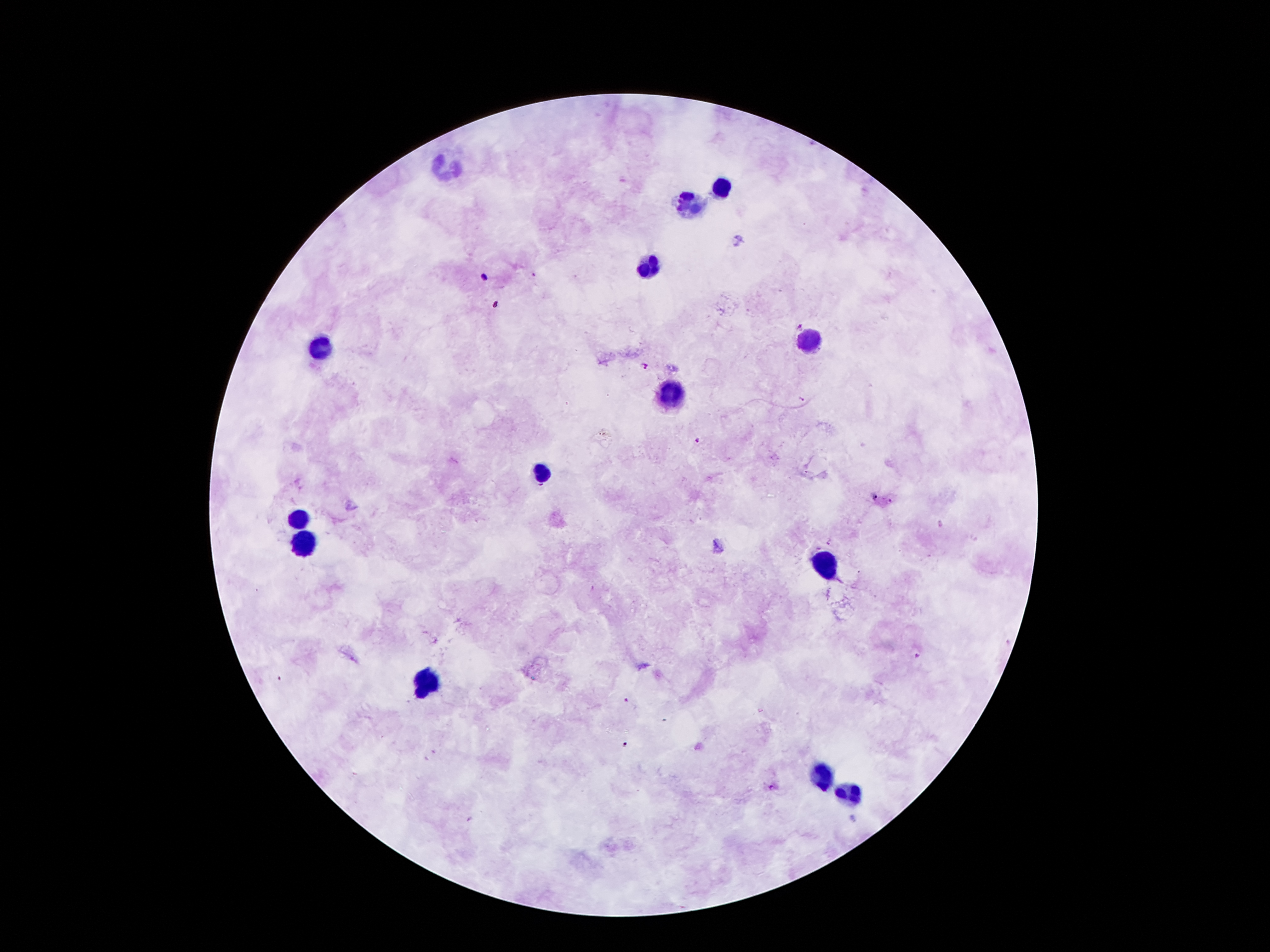
Approximate centers as [x, y] in pixels. Malaria parasite locations: [484, 276], [800, 325], [645, 368], [799, 398], [698, 441], [876, 498], [890, 501], [625, 701], [626, 742], [772, 789]. Leukocyte locations: [445, 166], [726, 188], [691, 206], [649, 263], [806, 338], [319, 349], [666, 391], [542, 473], [297, 517], [304, 541], [823, 559], [430, 685], [824, 776], [846, 793]. 100x magnification. Patient malaria status: infected with Plasmodium falciparum. Image is 1270×952 pixels. Giemsa-stained preparation. One field from this slide. Thick blood film. Photographed through the microscope eyepiece with a smartphone camera.